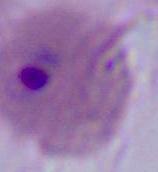
Summary:
  - Magnification: 400x or 1000x
  - Modality: micrograph
  - Identification: Plasmodium